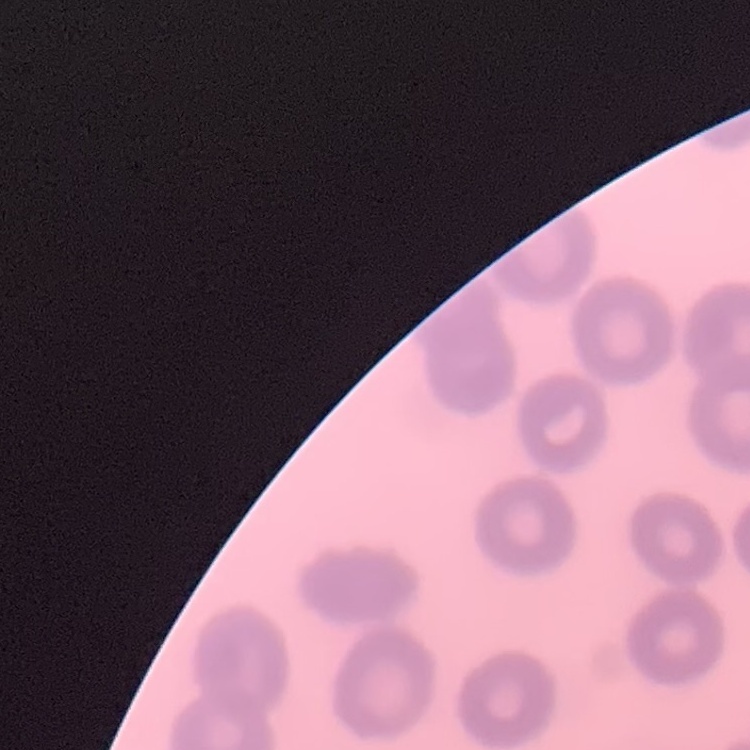

Summary:
  - Erythrocyte morphology: no rouleaux formation
  - Image type: square crop of a larger photomicrograph
  - Preparation: thin blood smear
  - Stain: Field's or Giemsa